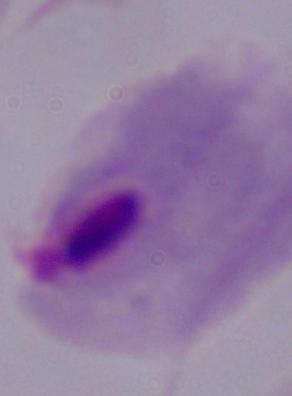
Summary:
  - Modality: micrograph
  - Identification: trichomonad
  - Magnification: 1000x